Comment on the morphology of the erythrocytes.
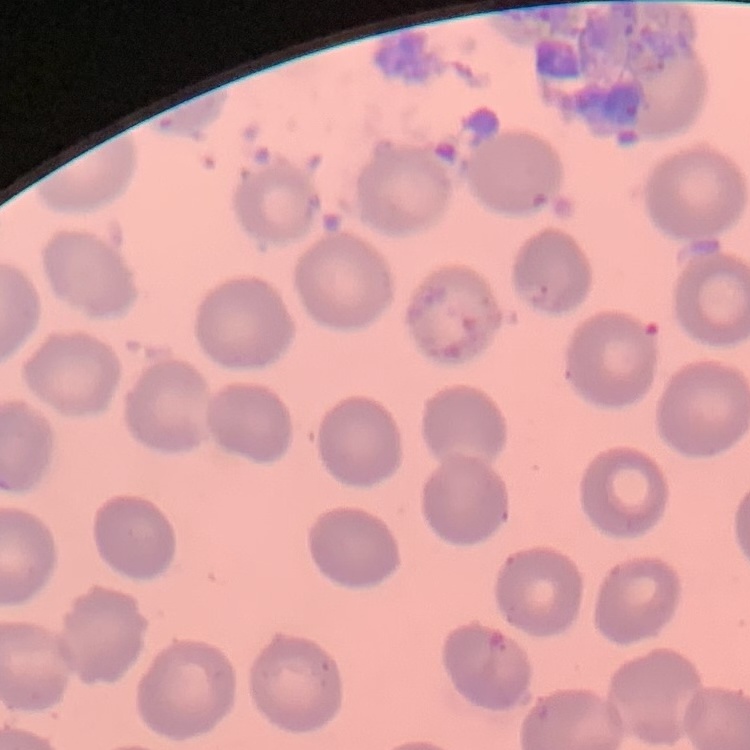
They show no rouleaux formation.

Stained with either Field's or Giemsa. Thin blood smear. Square crop of a larger photomicrograph.